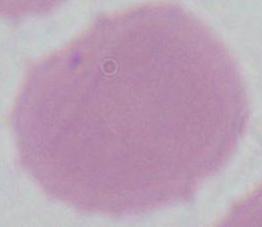
Summary:
  - Modality: photomicrograph
  - Identification: erythrocyte
  - Magnification: 1000x